Evaluate for malaria.
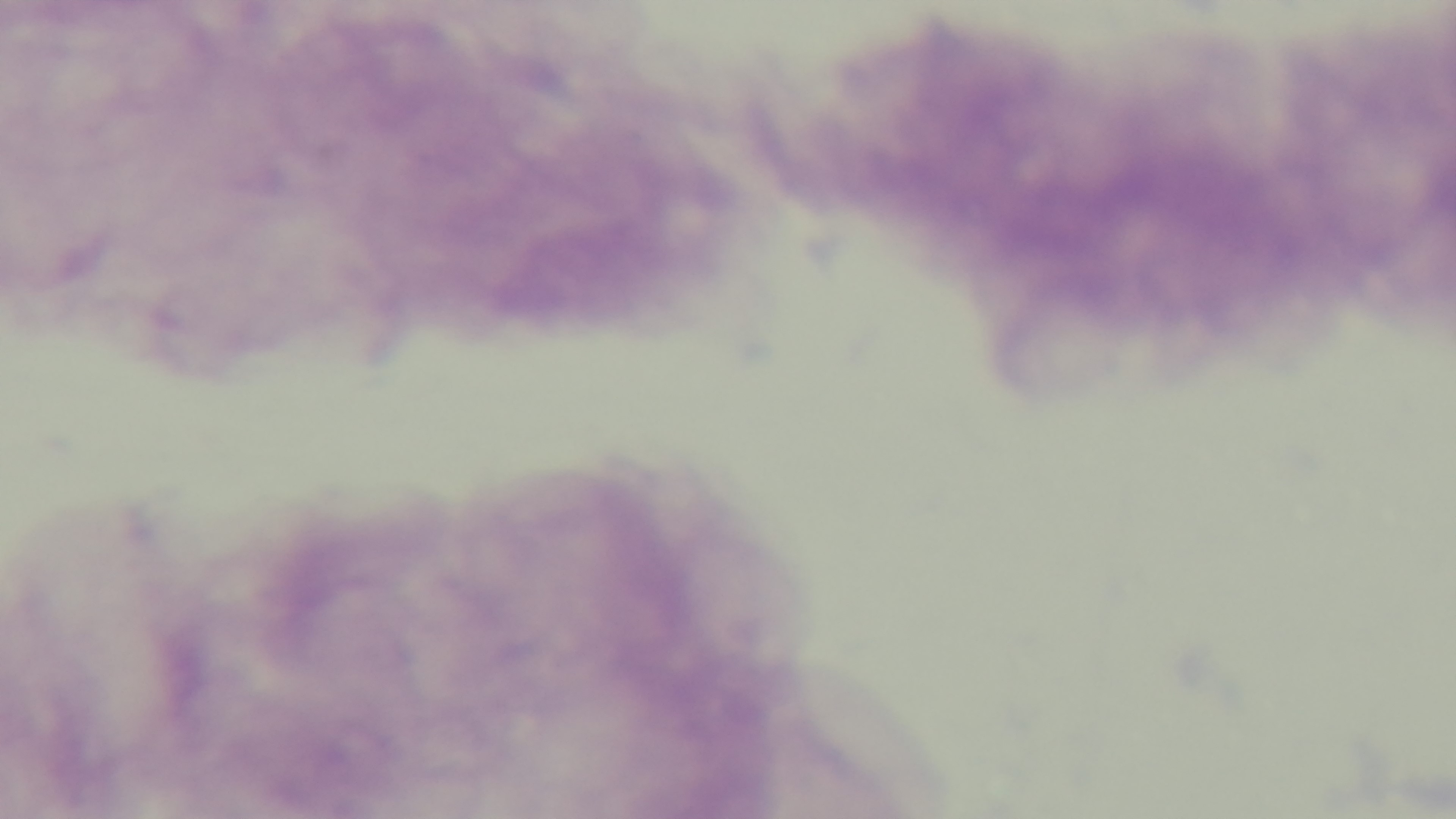
Negative.

capture: mounted 4K digital camera
preparation: thick blood film
field_of_view: single
objective: 100x oil immersion
modality: light microscopy
stain: Giemsa